Assess this cell for malaria.
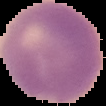

Uninfected.

preparation = thin blood smear
image size = 106×106 pixels
image type = segmented cell region on a black background